State which parasite is depicted.
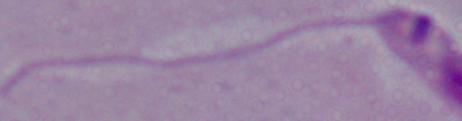

Leishmania.

Summary:
  - Modality: photomicrograph
  - Magnification: 1000x